Name the parasite shown.
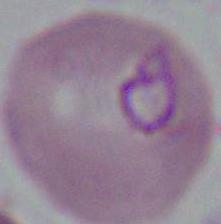

Plasmodium.

Micrograph. Captured at either 400x or 1000x magnification.